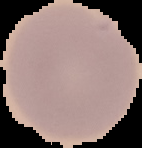 Image is 142×148 pixels. From a thin blood film. Segmented cell region on a black background. Result: no Plasmodium parasites seen.